Assess this cell for malaria.
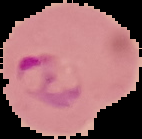

It is parasitized.

image type = segmented cell region on a black background
image size = 142×139 pixels
preparation = thin blood film